Point out each Plasmodium parasite.
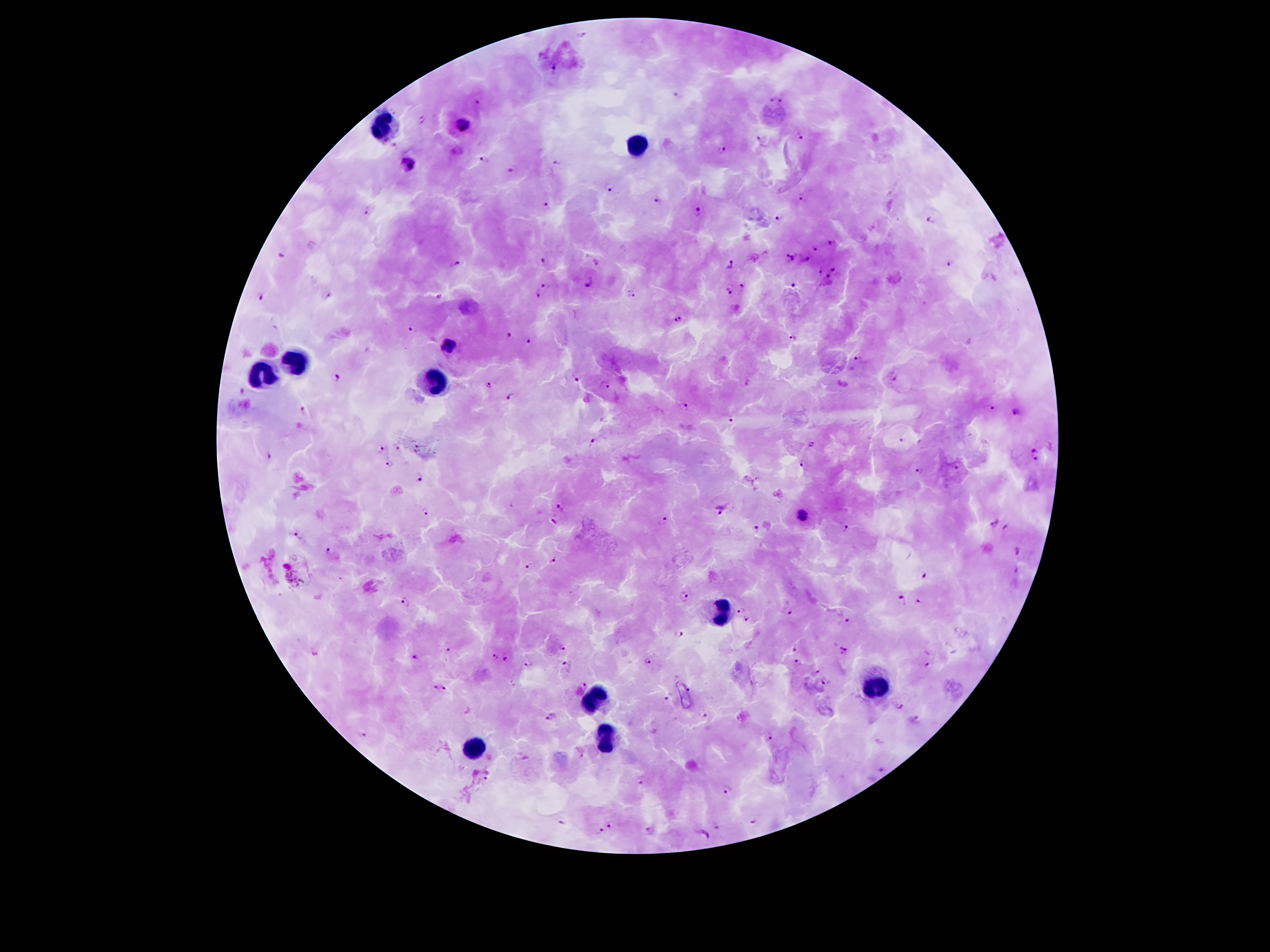
Approximate centers as {x, y} in pixels.
Plasmodium parasites: {553, 68}, {676, 95}, {778, 95}, {477, 101}, {421, 120}, {463, 126}, {801, 136}, {760, 141}, {394, 147}, {721, 151}, {485, 158}, {556, 162}, {410, 165}, {511, 171}, {609, 190}, {803, 198}, {658, 201}, {548, 205}, {367, 211}, {698, 211}, {779, 219}, {930, 221}, {831, 242}, {816, 248}, {281, 254}, {787, 257}, {542, 259}, {733, 261}, {804, 261}, {454, 264}, {948, 265}, {834, 270}, {819, 273}, {828, 278}, {544, 284}, {589, 284}, {792, 284}, {742, 286}, {728, 292}, {538, 293}, {261, 296}, {329, 296}, {630, 296}, {438, 299}, {677, 319}, {413, 328}, {509, 336}, {791, 337}, {528, 341}, {449, 344}, {858, 359}, {337, 376}, {895, 377}, {577, 378}, {487, 384}, {606, 386}, {242, 391}, {508, 398}, {684, 407}, {991, 407}, {303, 409}, {1016, 412}, {731, 418}, {902, 440}, {920, 441}, {593, 443}, {812, 445}, {397, 448}, {380, 449}, {419, 449}, {1035, 449}, {269, 457}, {1035, 459}, {390, 463}, {959, 463}, {802, 464}, {919, 470}, {419, 477}, {560, 506}, {719, 507}, {425, 511}, {803, 516}, {553, 520}, {664, 521}, {993, 522}, {757, 528}, {846, 528}, {1006, 528}, {298, 536}, {1018, 550}, {329, 551}, {553, 559}, {528, 564}, {1015, 572}, {925, 575}, {683, 595}, {406, 600}, {900, 600}, {918, 602}, {739, 609}, {790, 610}, {745, 619}, {849, 621}, {680, 634}, {792, 647}, {448, 648}, {562, 649}, {843, 649}, {315, 651}, {494, 655}, {413, 656}, {506, 658}, {649, 661}, {799, 663}, {925, 663}, {528, 664}, {567, 667}, {815, 672}, {825, 684}, {582, 685}, {435, 686}, {445, 687}, {689, 689}, {668, 697}, {900, 707}, {702, 714}, {550, 716}, {917, 719}, {363, 734}, {773, 736}, {879, 741}, {881, 771}, {487, 778}, {642, 782}, {726, 788}, {753, 820}, {561, 822}, {609, 825}, {715, 826}, {649, 829}, {601, 833}, {703, 837}.

Leukocyte locations: {381, 126}, {638, 146}, {297, 361}, {263, 375}, {433, 383}, {720, 611}, {873, 687}, {592, 699}, {604, 741}, {473, 751}. One field from this slide. Image is 1270×952 pixels. Giemsa-stained preparation. Photographed through the microscope eyepiece with a smartphone camera. 100x magnification. Patient malaria status: infected with Plasmodium falciparum. Thick blood film.